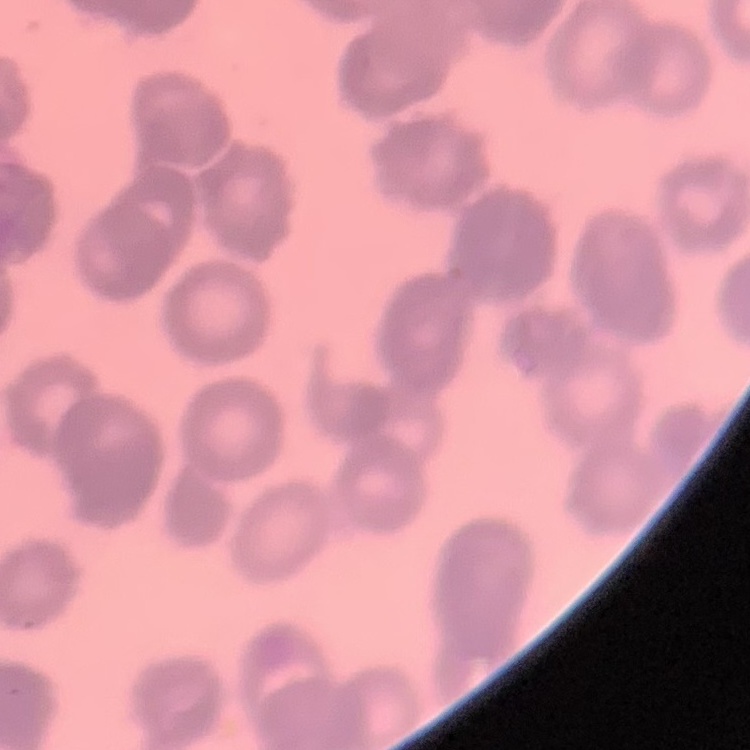

erythrocyte_morphology: rouleaux formation
stain: Field's or Giemsa
image_type: square crop of a larger photomicrograph
preparation: thin peripheral smear